Identify the cell.
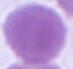
This is an erythrocyte.

magnification: 1000x
modality: micrograph